Assess this cell for malaria.
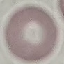
Uninfected.

image type = automatically extracted cell patch, resized to 64 × 64 pixels
preparation = thin blood smear
stain = Giemsa
capture = smartphone camera at the microscope eyepiece